Assess this cell for malaria.
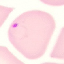

Parasitized.

Summary:
  - Preparation: thin blood film
  - Image type: automatically extracted cell patch, resized to 64 × 64 pixels
  - Stain: Giemsa
  - Capture: smartphone camera at the microscope eyepiece